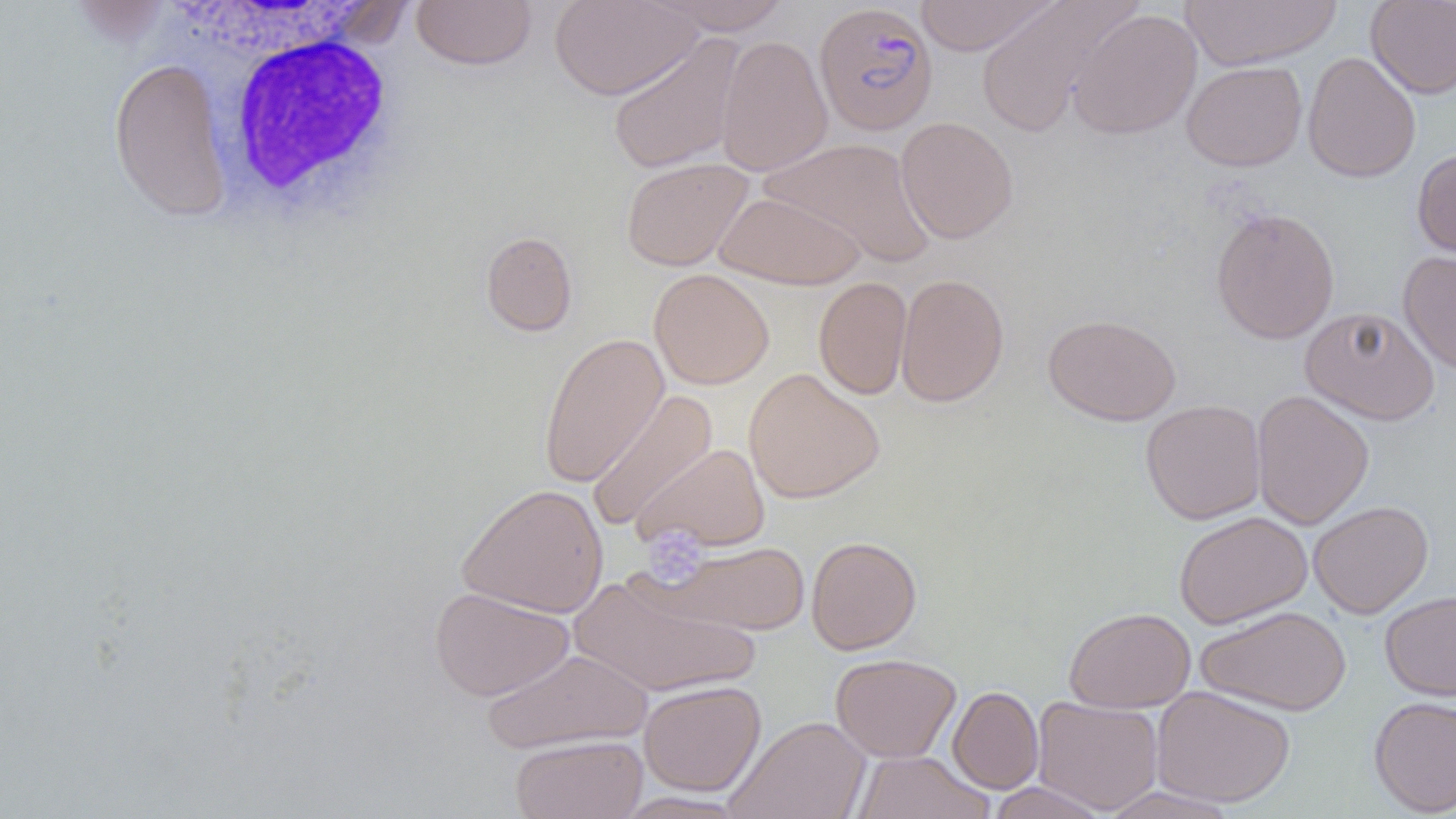

slide_level_diagnosis: Plasmodium falciparum
uninfected_red_blood_cell_locations: 'approximate bounding boxes as [x1, y1, x2, y2] in pixels: [411, 0, 537, 70], [549, 0, 702, 100], [646, 0, 793, 35], [913, 0, 1060, 56], [1180, 0, 1341, 70], [1365, 0, 1456, 99], [65, 1, 177, 48], [973, 1, 1139, 135], [1069, 9, 1202, 139], [607, 33, 746, 174], [716, 34, 833, 176], [1302, 51, 1421, 184], [108, 57, 234, 222], [1181, 61, 1307, 171], [895, 116, 1019, 244], [761, 137, 935, 267], [1412, 147, 1456, 260], [621, 157, 753, 271], [715, 190, 866, 290], [1210, 207, 1340, 344], [481, 231, 578, 337], [1398, 250, 1456, 374], [649, 268, 774, 390], [895, 273, 1010, 407], [813, 276, 913, 399], [1300, 306, 1440, 425], [1042, 313, 1182, 426], [538, 333, 669, 488], [743, 368, 885, 504], [586, 389, 717, 533], [1250, 390, 1374, 529], [1140, 399, 1266, 524], [631, 443, 771, 554], [457, 483, 609, 618], [1308, 500, 1433, 618], [1174, 510, 1312, 629], [806, 536, 922, 654], [658, 540, 810, 635], [567, 572, 760, 698], [430, 586, 574, 701], [1380, 590, 1456, 701], [1196, 605, 1351, 716], [1064, 607, 1196, 712], [482, 648, 652, 754], [831, 653, 961, 762], [639, 680, 766, 795], [1151, 685, 1295, 808], [947, 686, 1044, 794], [1368, 696, 1456, 817], [1032, 697, 1163, 814], [725, 715, 871, 819], [510, 734, 648, 819], [852, 751, 994, 819], [986, 782, 1112, 819], [1097, 786, 1242, 819]'
modality: light microscopy
plasmodium_falciparum_infected_red_blood_cell_locations: 'approximate bounding boxes as [x1, y1, x2, y2] in pixels: [814, 3, 938, 136]'
white_blood_cell_locations: 'approximate bounding boxes as [x1, y1, x2, y2] in pixels: [203, 24, 413, 231]'
field_of_view: one of a larger specimen
platelet_locations: 'approximate bounding boxes as [x1, y1, x2, y2] in pixels: [640, 528, 708, 587]'
preparation: thin blood film
magnification: 1000x
image_size: 1456×819 pixels